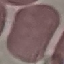

Result: no malaria parasites seen. Cell patch, automatically extracted from a larger field of view and resized to 64 × 64 pixels. Acquired by smartphone through the microscope eyepiece. Giemsa stain. Thin smear of blood.